Classify this cell by malaria status.
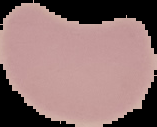
It is uninfected.

Summary:
  - Image type: segmented cell region with the area outside set to black
  - Image size: 157×127 pixels
  - Preparation: thin blood film